Identify the parasite.
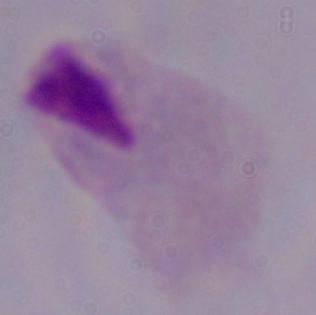
A trichomonad.

Summary:
  - Modality: photomicrograph
  - Magnification: 1000x